Describe the morphology of the erythrocytes.
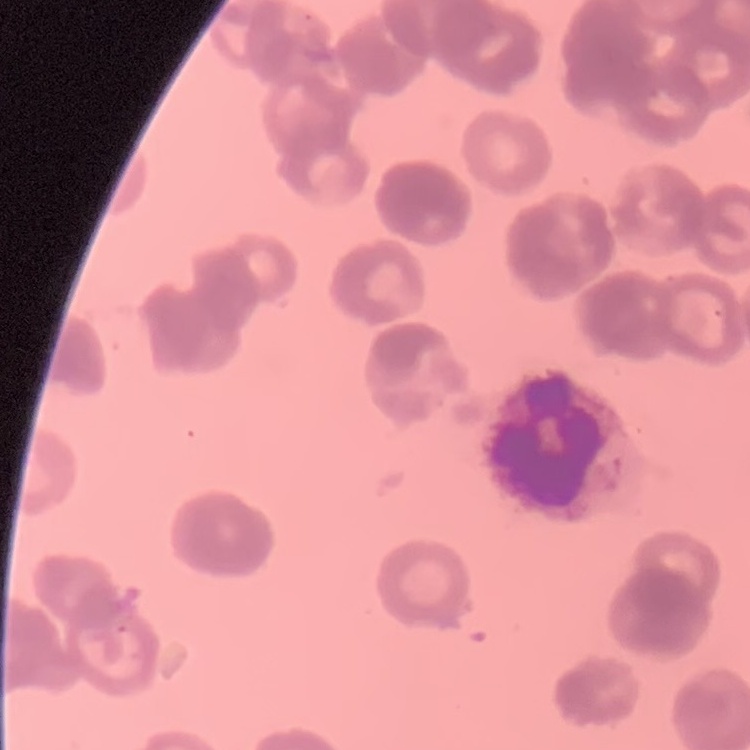

They show rouleaux formation.

image type = square crop of a larger photomicrograph
preparation = thin blood smear
stain = Field's or Giemsa